Assess for Plasmodium parasites.
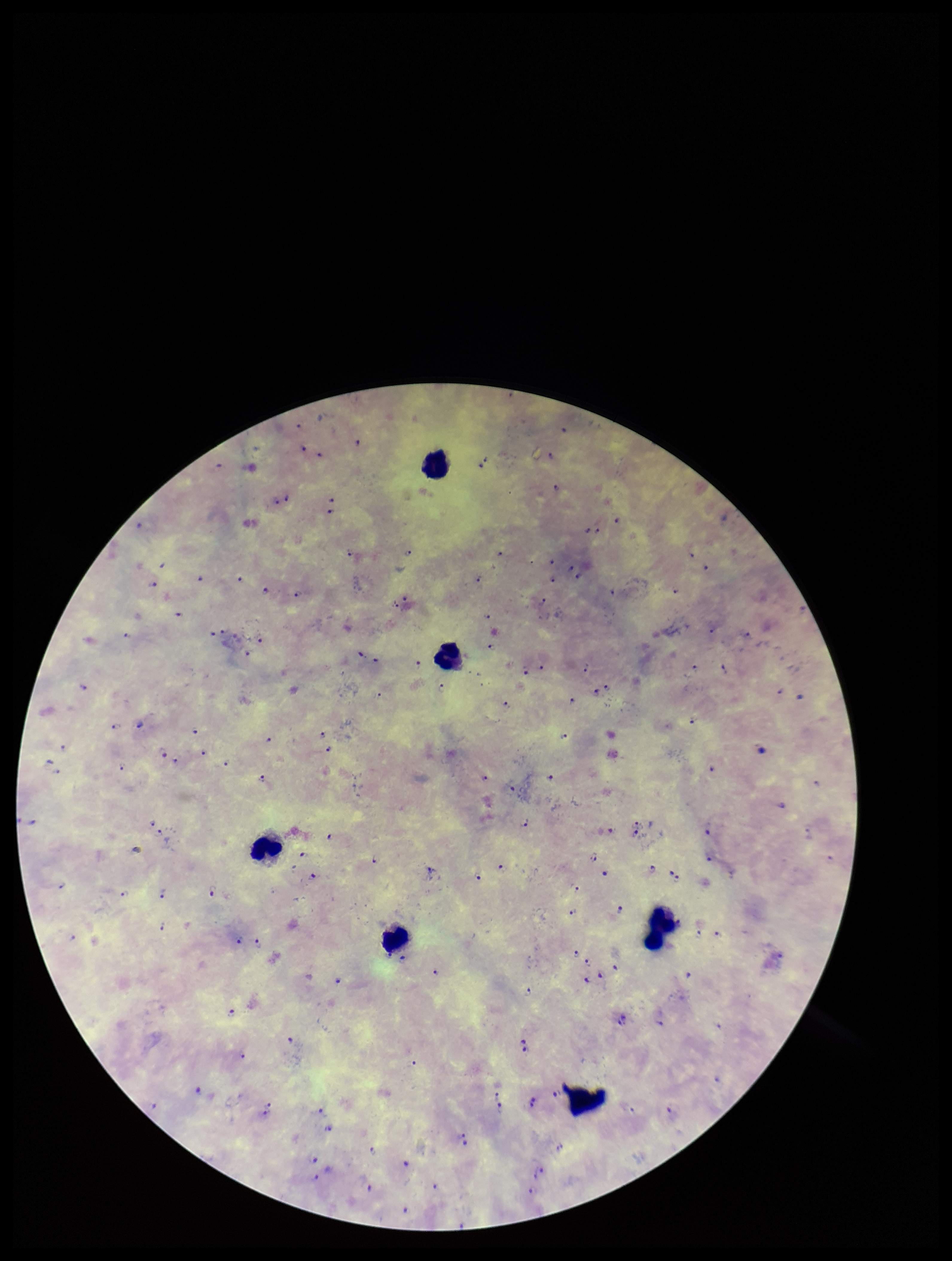
Identified.

Summary:
  - Image size: 952×1261 pixels
  - Field of view: single
  - Leukocyte count: 6
  - Preparation: thick
  - Capture: smartphone photograph through the microscope eyepiece
  - Stain: Giemsa
  - Species reported for this patient: Plasmodium falciparum
  - Parasite count: 112
  - Patient malaria status: positive